Give the position of every Plasmodium parasite.
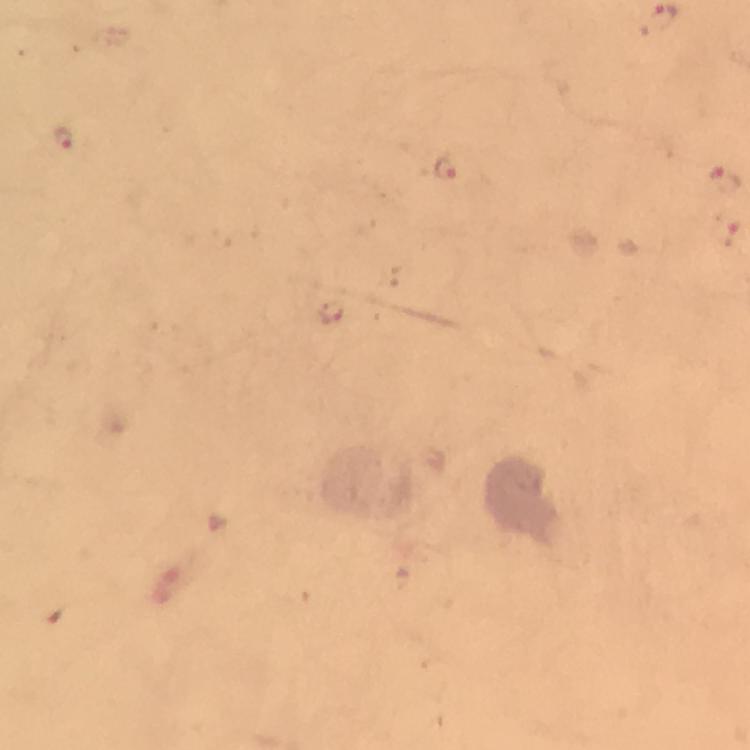
Approximate centers as {x, y} in pixels.
Plasmodium parasites: {63, 137}, {447, 168}, {722, 181}, {726, 230}, {328, 310}.

context: from a diagnostic examination for malaria
stain: Giemsa
preparation: thick blood film
cropped_from: a single field of view
magnification: 100x
image_size: 750×750 pixels
capture: smartphone camera through the microscope
immersion_oil: applied